Identify the cell.
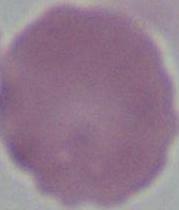

This is an erythrocyte.

Micrograph. Captured at 1000x magnification.